State the blood parasite species.
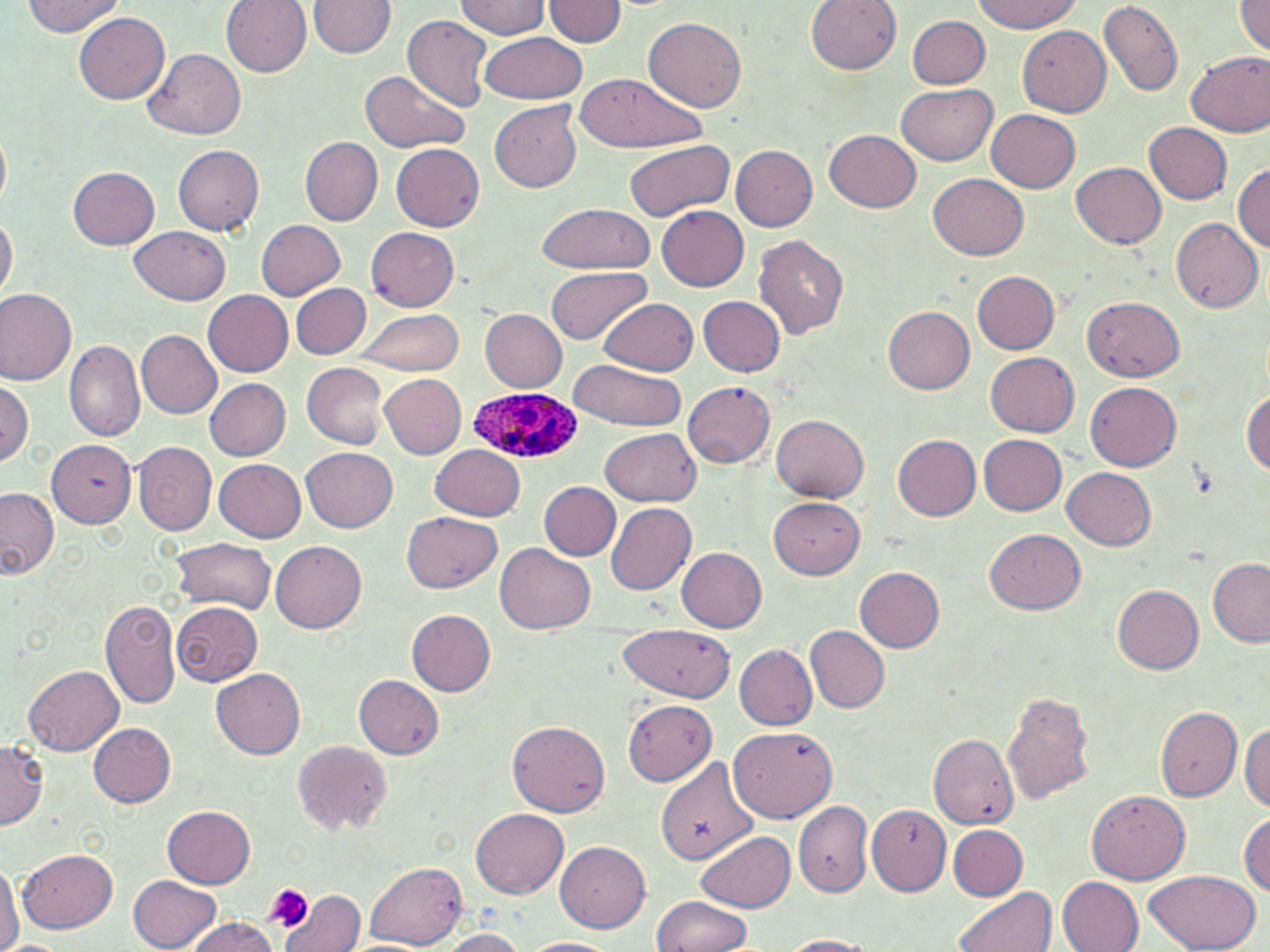

Plasmodium ovale.

Approximate bounding boxes as [x1, y1, x2, y2] in pixels. Plasmodium ovale-infected red blood cell locations: [468, 387, 581, 465]. Uninfected red blood cell locations: [23, 0, 125, 37], [221, 0, 313, 76], [308, 0, 396, 59], [454, 0, 550, 39], [543, 0, 626, 45], [806, 0, 901, 73], [969, 0, 1085, 34], [1099, 1, 1184, 97], [1235, 1, 1270, 58], [74, 13, 169, 104], [402, 15, 494, 111], [907, 15, 990, 87], [643, 17, 747, 111], [1018, 25, 1112, 116], [481, 32, 586, 103], [146, 48, 247, 140], [1185, 50, 1270, 137], [359, 69, 468, 153], [573, 72, 706, 153], [898, 84, 996, 165], [490, 101, 581, 193], [987, 109, 1080, 192], [1143, 121, 1232, 203], [825, 128, 920, 212], [0, 130, 10, 208], [301, 137, 383, 225], [623, 140, 732, 222], [391, 142, 485, 230], [732, 143, 817, 230], [173, 145, 264, 235], [1071, 161, 1165, 248], [1233, 165, 1270, 251], [69, 167, 159, 249], [929, 173, 1028, 260], [535, 203, 654, 274], [657, 205, 748, 291], [0, 212, 17, 304], [1171, 218, 1262, 311], [256, 219, 347, 300], [131, 225, 231, 305], [367, 228, 459, 311], [753, 235, 850, 341], [547, 266, 650, 346], [972, 271, 1060, 353], [292, 284, 371, 358], [0, 289, 77, 387], [204, 291, 292, 375], [1084, 295, 1184, 382], [699, 296, 784, 376], [598, 297, 697, 377], [883, 306, 974, 393], [354, 308, 463, 375], [481, 309, 567, 392], [137, 330, 222, 418], [64, 340, 144, 441], [986, 352, 1078, 436], [567, 360, 686, 430], [303, 362, 388, 450], [379, 374, 465, 460], [205, 378, 291, 460], [0, 379, 33, 467], [1084, 379, 1181, 470], [682, 380, 776, 467], [1242, 391, 1270, 474], [772, 413, 869, 500], [602, 428, 700, 506], [978, 434, 1067, 515], [893, 435, 981, 520], [46, 439, 135, 526], [135, 441, 216, 534], [431, 445, 525, 520], [302, 447, 397, 532], [214, 458, 306, 542], [1062, 469, 1156, 549], [539, 481, 621, 560], [0, 487, 58, 579], [768, 495, 865, 578], [605, 503, 697, 594], [402, 510, 502, 593], [985, 529, 1085, 614], [171, 538, 277, 613], [271, 541, 366, 632], [497, 543, 595, 635], [677, 547, 767, 632], [1208, 560, 1270, 647], [855, 567, 944, 651], [1111, 584, 1204, 674], [101, 600, 180, 709], [172, 601, 263, 685], [407, 609, 496, 695], [618, 624, 735, 700], [806, 625, 889, 712], [733, 643, 817, 730], [24, 665, 125, 756], [211, 668, 306, 757], [354, 673, 445, 760], [1003, 690, 1097, 806], [622, 699, 717, 785], [1155, 706, 1242, 801], [508, 719, 611, 817], [1240, 722, 1270, 813], [89, 723, 176, 806], [728, 724, 839, 822], [927, 733, 1019, 829], [0, 739, 48, 829], [293, 741, 390, 832], [657, 757, 759, 866], [1086, 788, 1190, 884], [794, 799, 872, 896], [163, 803, 257, 889], [867, 806, 951, 896], [471, 808, 568, 897], [1238, 812, 1270, 896], [949, 824, 1028, 899], [698, 831, 795, 913], [555, 841, 651, 932], [17, 849, 117, 933], [0, 860, 22, 952], [365, 863, 467, 947], [1143, 869, 1261, 952], [130, 875, 221, 951], [1058, 876, 1143, 952], [954, 886, 1057, 952], [281, 887, 367, 952], [652, 895, 753, 951], [185, 917, 280, 952], [436, 928, 530, 951], [781, 935, 876, 952], [521, 938, 619, 952]. Platelet locations: [264, 885, 313, 931]. Image is 1270×952 pixels. Thin blood film. May-Grünwald-Giemsa stain. Light microscopy. Single field of view. Captured at 1000x magnification.